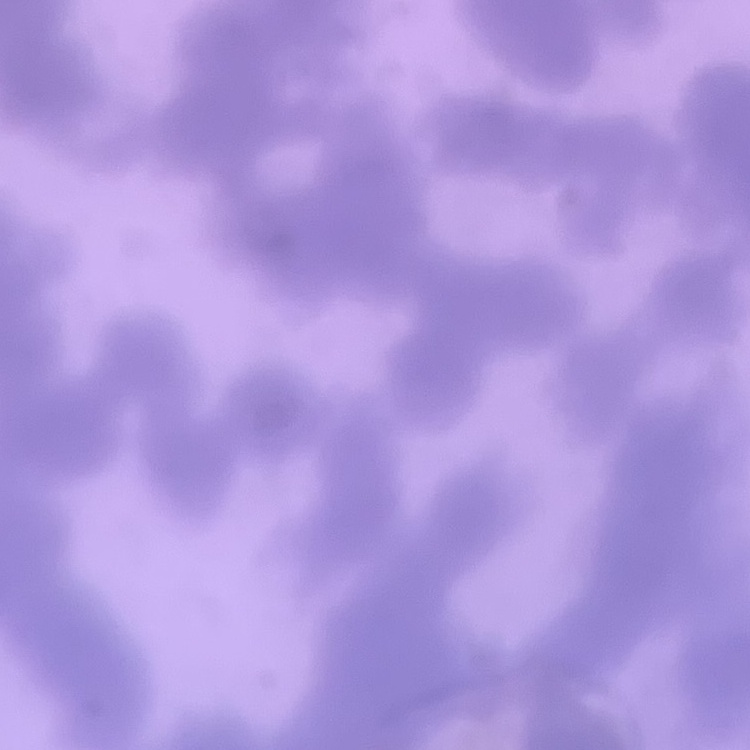
red_blood_cell_morphology: rouleaux formation
preparation: thin peripheral smear
image_type: one tile cut from a larger photomicrograph
stain: Field's or Giemsa